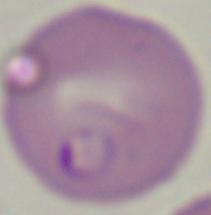
Summary:
  - Identification: Babesia
  - Modality: photomicrograph
  - Magnification: 1000x